Identify the parasite.
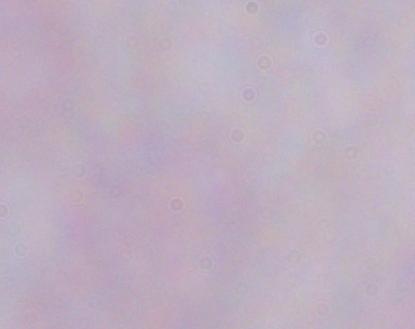

A trypanosome.

modality = photomicrograph
magnification = 1000x